Comment on the morphology of the red blood cells.
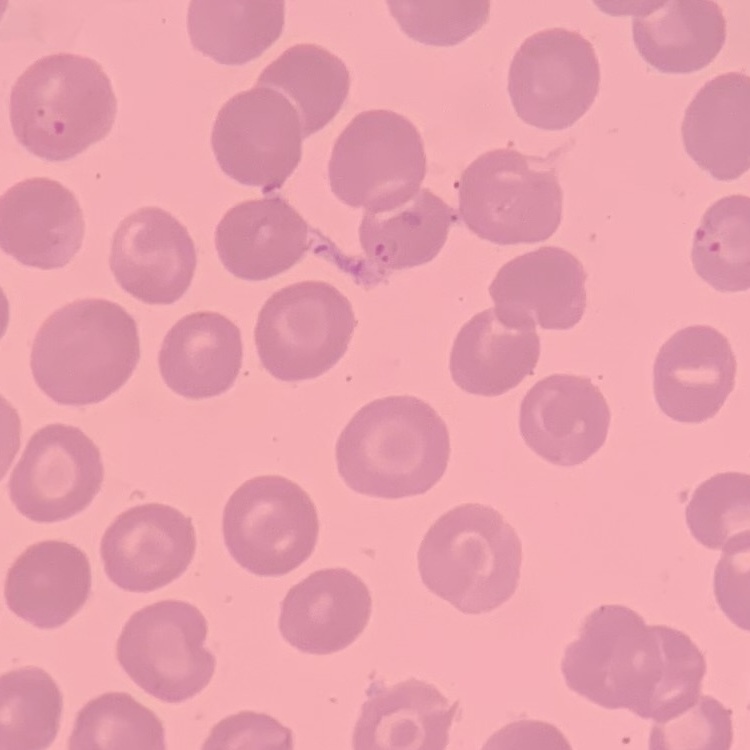

No rouleaux formation.

Field's or Giemsa stain. One tile cut from a larger photomicrograph. Thin blood smear.